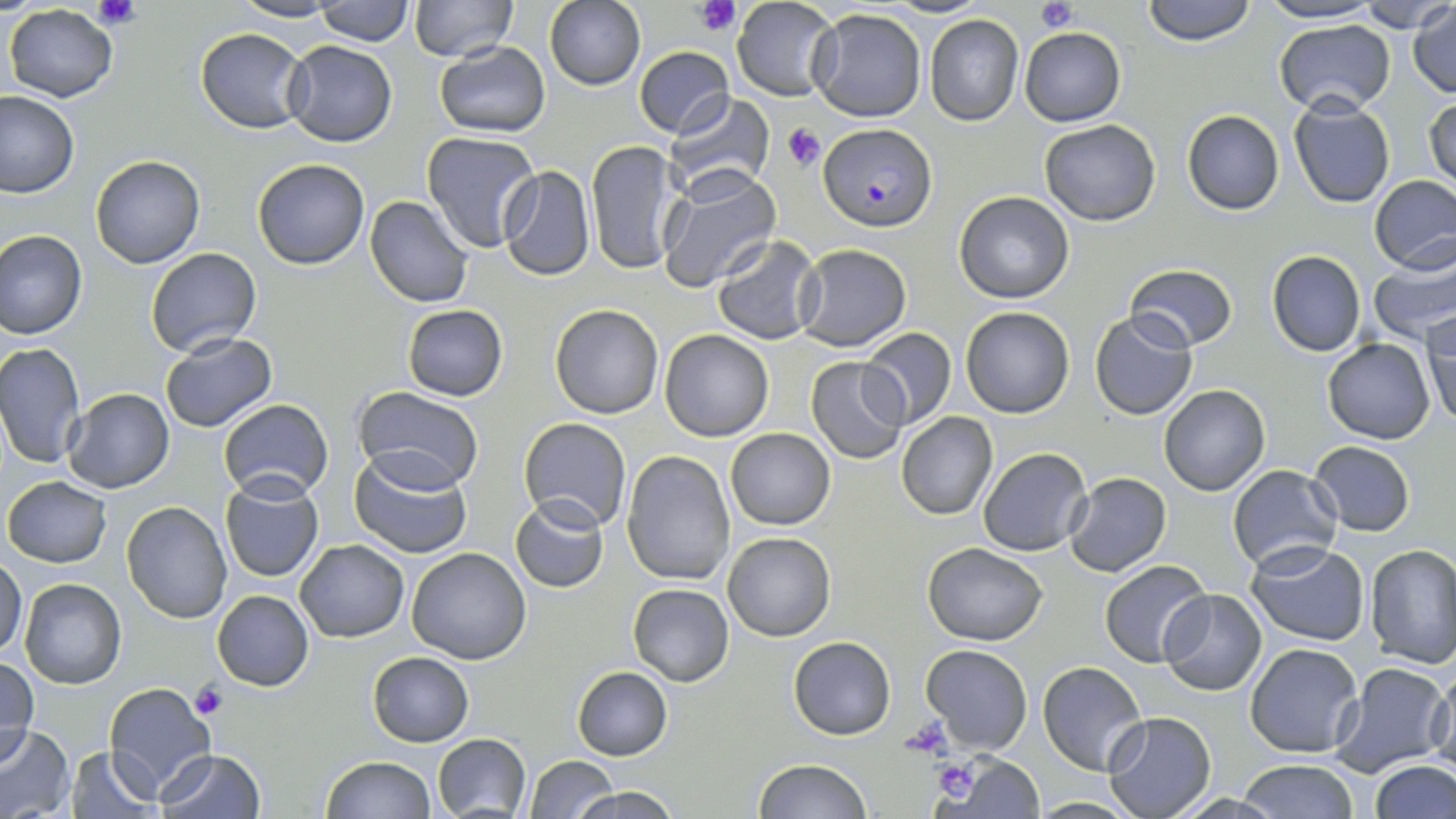

{
  "slide_level_diagnosis": "Plasmodium falciparum",
  "platelet_locations": "approximate bounding boxes as named x1/y1/x2/y2 corners in pixels: (x1=91, y1=0, x2=143, y2=31), (x1=695, y1=0, x2=741, y2=34), (x1=1034, y1=0, x2=1079, y2=29), (x1=783, y1=123, x2=826, y2=171), (x1=190, y1=682, x2=227, y2=718), (x1=901, y1=715, x2=952, y2=761), (x1=934, y1=758, x2=980, y2=800)",
  "magnification": "1000x",
  "plasmodium_falciparum_infected_red_blood_cell_locations": "approximate bounding boxes as named x1/y1/x2/y2 corners in pixels: (x1=819, y1=123, x2=936, y2=229)",
  "image_size": "1456×819 pixels",
  "preparation": "thin blood smear",
  "field_of_view": "single",
  "stain": "May-Grünwald-Giemsa",
  "modality": "optical microscopy",
  "uninfected_red_blood_cell_locations": "approximate bounding boxes as named x1/y1/x2/y2 corners in pixels: (x1=231, y1=0, x2=346, y2=23), (x1=315, y1=0, x2=413, y2=45), (x1=409, y1=0, x2=517, y2=63), (x1=732, y1=0, x2=839, y2=101), (x1=1141, y1=0, x2=1256, y2=45), (x1=1355, y1=0, x2=1456, y2=32), (x1=543, y1=1, x2=645, y2=91), (x1=1255, y1=1, x2=1385, y2=25), (x1=1408, y1=4, x2=1456, y2=98), (x1=5, y1=6, x2=117, y2=103), (x1=807, y1=8, x2=926, y2=122), (x1=923, y1=14, x2=1025, y2=127), (x1=1273, y1=18, x2=1396, y2=116), (x1=195, y1=28, x2=309, y2=132), (x1=1019, y1=28, x2=1125, y2=126), (x1=281, y1=41, x2=397, y2=147), (x1=433, y1=42, x2=551, y2=137), (x1=633, y1=44, x2=735, y2=139), (x1=661, y1=89, x2=776, y2=198), (x1=0, y1=93, x2=79, y2=197), (x1=1425, y1=96, x2=1456, y2=192), (x1=1287, y1=99, x2=1395, y2=208), (x1=1181, y1=109, x2=1285, y2=215), (x1=1039, y1=119, x2=1161, y2=226), (x1=422, y1=132, x2=542, y2=254), (x1=586, y1=140, x2=683, y2=276), (x1=90, y1=155, x2=206, y2=268), (x1=253, y1=159, x2=372, y2=270), (x1=496, y1=166, x2=596, y2=281), (x1=657, y1=166, x2=782, y2=291), (x1=1369, y1=175, x2=1456, y2=273), (x1=954, y1=191, x2=1074, y2=304), (x1=365, y1=196, x2=475, y2=307), (x1=0, y1=229, x2=88, y2=340), (x1=711, y1=235, x2=826, y2=346), (x1=793, y1=244, x2=912, y2=350), (x1=146, y1=247, x2=262, y2=356), (x1=1266, y1=250, x2=1367, y2=357), (x1=1369, y1=251, x2=1456, y2=345), (x1=1124, y1=263, x2=1239, y2=351), (x1=550, y1=303, x2=664, y2=419), (x1=402, y1=304, x2=508, y2=401), (x1=960, y1=307, x2=1074, y2=418), (x1=1089, y1=309, x2=1198, y2=421), (x1=1423, y1=310, x2=1456, y2=427), (x1=858, y1=327, x2=957, y2=431), (x1=660, y1=330, x2=774, y2=442), (x1=159, y1=331, x2=278, y2=433), (x1=1323, y1=339, x2=1435, y2=443), (x1=0, y1=343, x2=85, y2=469), (x1=805, y1=355, x2=910, y2=463), (x1=1159, y1=385, x2=1269, y2=495), (x1=353, y1=386, x2=483, y2=490), (x1=61, y1=388, x2=176, y2=493), (x1=218, y1=398, x2=334, y2=500), (x1=896, y1=412, x2=997, y2=520), (x1=520, y1=417, x2=632, y2=531), (x1=725, y1=428, x2=835, y2=530), (x1=1308, y1=440, x2=1416, y2=535), (x1=979, y1=447, x2=1092, y2=556), (x1=622, y1=449, x2=738, y2=585), (x1=350, y1=453, x2=471, y2=558), (x1=1227, y1=465, x2=1343, y2=572), (x1=1063, y1=472, x2=1172, y2=576), (x1=219, y1=475, x2=325, y2=584), (x1=4, y1=476, x2=111, y2=566), (x1=511, y1=495, x2=607, y2=592), (x1=121, y1=500, x2=232, y2=622), (x1=723, y1=531, x2=835, y2=641), (x1=295, y1=538, x2=408, y2=641), (x1=1246, y1=540, x2=1370, y2=645), (x1=923, y1=541, x2=1048, y2=646), (x1=1365, y1=543, x2=1456, y2=668), (x1=405, y1=548, x2=531, y2=664), (x1=0, y1=556, x2=26, y2=659), (x1=1099, y1=559, x2=1213, y2=669), (x1=21, y1=578, x2=127, y2=689), (x1=627, y1=583, x2=734, y2=685), (x1=1160, y1=588, x2=1268, y2=695), (x1=211, y1=591, x2=315, y2=692), (x1=788, y1=636, x2=896, y2=740), (x1=1245, y1=641, x2=1364, y2=757), (x1=920, y1=644, x2=1033, y2=752), (x1=368, y1=651, x2=474, y2=747), (x1=0, y1=659, x2=38, y2=760), (x1=1038, y1=660, x2=1147, y2=774), (x1=1331, y1=662, x2=1451, y2=776), (x1=1427, y1=663, x2=1456, y2=773), (x1=573, y1=666, x2=672, y2=760), (x1=103, y1=681, x2=215, y2=798), (x1=1102, y1=711, x2=1216, y2=817), (x1=1352, y1=717, x2=1454, y2=816), (x1=1, y1=728, x2=75, y2=816), (x1=431, y1=733, x2=533, y2=818), (x1=64, y1=747, x2=161, y2=818), (x1=157, y1=749, x2=266, y2=819), (x1=948, y1=752, x2=1046, y2=818), (x1=320, y1=756, x2=435, y2=818), (x1=526, y1=756, x2=618, y2=819), (x1=754, y1=759, x2=871, y2=819), (x1=1238, y1=760, x2=1359, y2=818), (x1=1371, y1=760, x2=1455, y2=819), (x1=568, y1=786, x2=681, y2=819), (x1=1028, y1=797, x2=1146, y2=816)"
}